Report the malaria status of this cell.
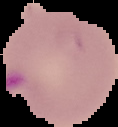
Parasitized.

Summary:
  - Image type: cell region segmented out of the field of view; surrounding area masked to black
  - Image size: 118×127 pixels
  - Preparation: thin blood smear